Assess this cell for malaria.
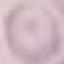

Uninfected.

Photographed with a smartphone camera at the microscope eyepiece. Giemsa-stained preparation. Thin blood smear. Cell patch, automatically extracted from a larger field of view and resized to 64 × 64 pixels.